Outline each Plasmodium falciparum-infected red blood cell.
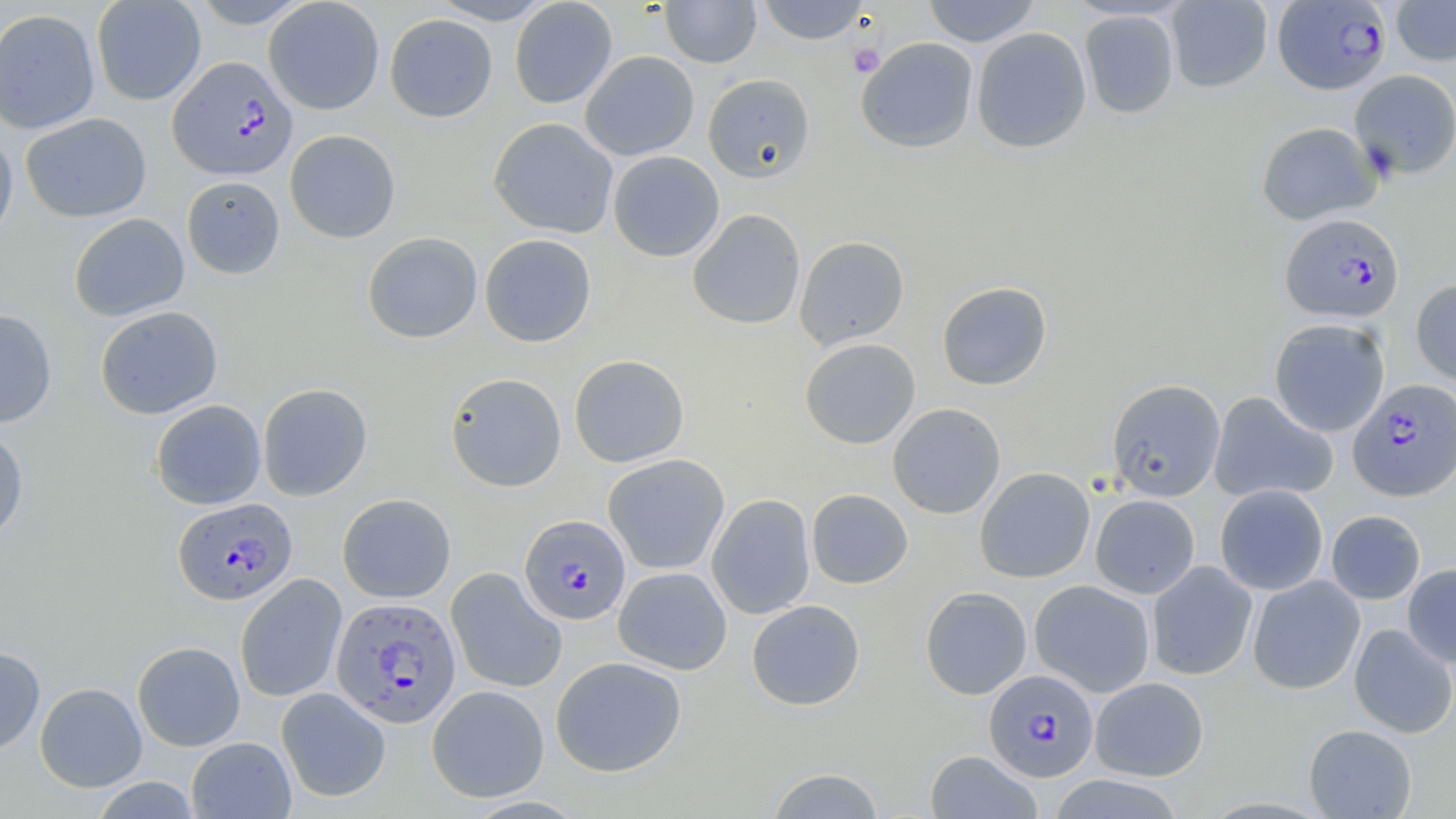

Approximate bounding boxes as named x1/y1/x2/y2 corners in pixels.
Plasmodium falciparum-infected red blood cells: (x1=1275, y1=1, x2=1395, y2=95), (x1=168, y1=55, x2=298, y2=180), (x1=1280, y1=212, x2=1405, y2=324), (x1=1347, y1=378, x2=1456, y2=502), (x1=173, y1=497, x2=297, y2=605), (x1=519, y1=515, x2=631, y2=625), (x1=331, y1=596, x2=462, y2=727), (x1=984, y1=669, x2=1099, y2=781).

slide-level diagnosis = Plasmodium falciparum
image size = 1456×819 pixels
modality = light microscopy
uninfected red blood cell locations = approximate bounding boxes as named x1/y1/x2/y2 corners in pixels: (x1=91, y1=0, x2=206, y2=105), (x1=188, y1=0, x2=315, y2=28), (x1=430, y1=0, x2=555, y2=25), (x1=509, y1=0, x2=618, y2=108), (x1=660, y1=0, x2=761, y2=68), (x1=755, y1=0, x2=871, y2=45), (x1=922, y1=0, x2=1042, y2=47), (x1=1166, y1=0, x2=1273, y2=93), (x1=263, y1=1, x2=385, y2=114), (x1=1391, y1=1, x2=1456, y2=66), (x1=0, y1=8, x2=101, y2=135), (x1=1079, y1=10, x2=1179, y2=119), (x1=384, y1=14, x2=498, y2=123), (x1=971, y1=27, x2=1092, y2=153), (x1=856, y1=37, x2=978, y2=153), (x1=580, y1=51, x2=700, y2=161), (x1=1350, y1=70, x2=1456, y2=179), (x1=702, y1=73, x2=816, y2=183), (x1=20, y1=112, x2=152, y2=223), (x1=488, y1=117, x2=618, y2=238), (x1=1256, y1=121, x2=1382, y2=225), (x1=284, y1=129, x2=401, y2=243), (x1=0, y1=130, x2=18, y2=250), (x1=608, y1=151, x2=724, y2=261), (x1=181, y1=175, x2=285, y2=279), (x1=686, y1=209, x2=805, y2=330), (x1=69, y1=213, x2=190, y2=321), (x1=362, y1=232, x2=483, y2=343), (x1=480, y1=234, x2=597, y2=347), (x1=794, y1=235, x2=909, y2=349), (x1=1410, y1=279, x2=1456, y2=386), (x1=937, y1=281, x2=1052, y2=390), (x1=95, y1=305, x2=223, y2=419), (x1=0, y1=308, x2=57, y2=428), (x1=1269, y1=318, x2=1390, y2=437), (x1=799, y1=338, x2=921, y2=449), (x1=569, y1=354, x2=689, y2=467), (x1=445, y1=372, x2=567, y2=492), (x1=1106, y1=379, x2=1226, y2=501), (x1=258, y1=383, x2=372, y2=501), (x1=1209, y1=392, x2=1338, y2=503), (x1=150, y1=400, x2=266, y2=509), (x1=887, y1=402, x2=1006, y2=519), (x1=0, y1=426, x2=29, y2=544), (x1=603, y1=454, x2=729, y2=575), (x1=975, y1=467, x2=1095, y2=583), (x1=1214, y1=484, x2=1329, y2=595), (x1=806, y1=489, x2=913, y2=589), (x1=337, y1=494, x2=456, y2=602), (x1=707, y1=494, x2=816, y2=620), (x1=1090, y1=494, x2=1200, y2=599), (x1=1325, y1=510, x2=1425, y2=604), (x1=1147, y1=561, x2=1258, y2=680), (x1=1402, y1=563, x2=1456, y2=668), (x1=445, y1=567, x2=567, y2=693), (x1=613, y1=567, x2=732, y2=675), (x1=235, y1=574, x2=347, y2=702), (x1=1247, y1=575, x2=1365, y2=695), (x1=1029, y1=579, x2=1155, y2=697), (x1=920, y1=586, x2=1032, y2=700), (x1=746, y1=599, x2=866, y2=710), (x1=1349, y1=624, x2=1456, y2=738), (x1=132, y1=641, x2=245, y2=751), (x1=0, y1=646, x2=46, y2=755), (x1=550, y1=656, x2=686, y2=777), (x1=1090, y1=677, x2=1209, y2=781), (x1=35, y1=682, x2=147, y2=791), (x1=427, y1=685, x2=549, y2=802), (x1=276, y1=687, x2=391, y2=803), (x1=1303, y1=724, x2=1417, y2=818), (x1=186, y1=737, x2=296, y2=818), (x1=924, y1=750, x2=1043, y2=819), (x1=765, y1=767, x2=886, y2=818), (x1=1046, y1=774, x2=1185, y2=818), (x1=90, y1=776, x2=202, y2=819)
preparation = thin blood smear
magnification = 1000x
field of view = one of a larger specimen
platelet locations = approximate bounding boxes as named x1/y1/x2/y2 corners in pixels: (x1=848, y1=42, x2=886, y2=77)
stain = May-Grünwald-Giemsa